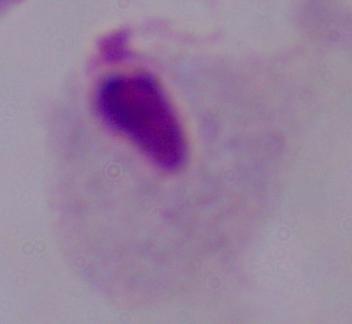

Summary:
  - Modality: photomicrograph
  - Magnification: 1000x
  - Identification: trichomonad